Name the parasite shown.
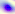
Toxoplasma gondii.

Micrograph. 400x magnification.